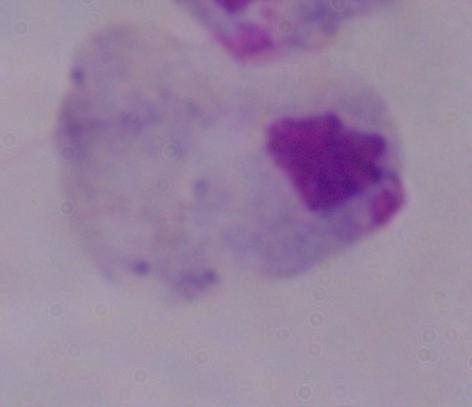
{
  "magnification": "1000x",
  "identification": "trichomonad",
  "modality": "micrograph"
}